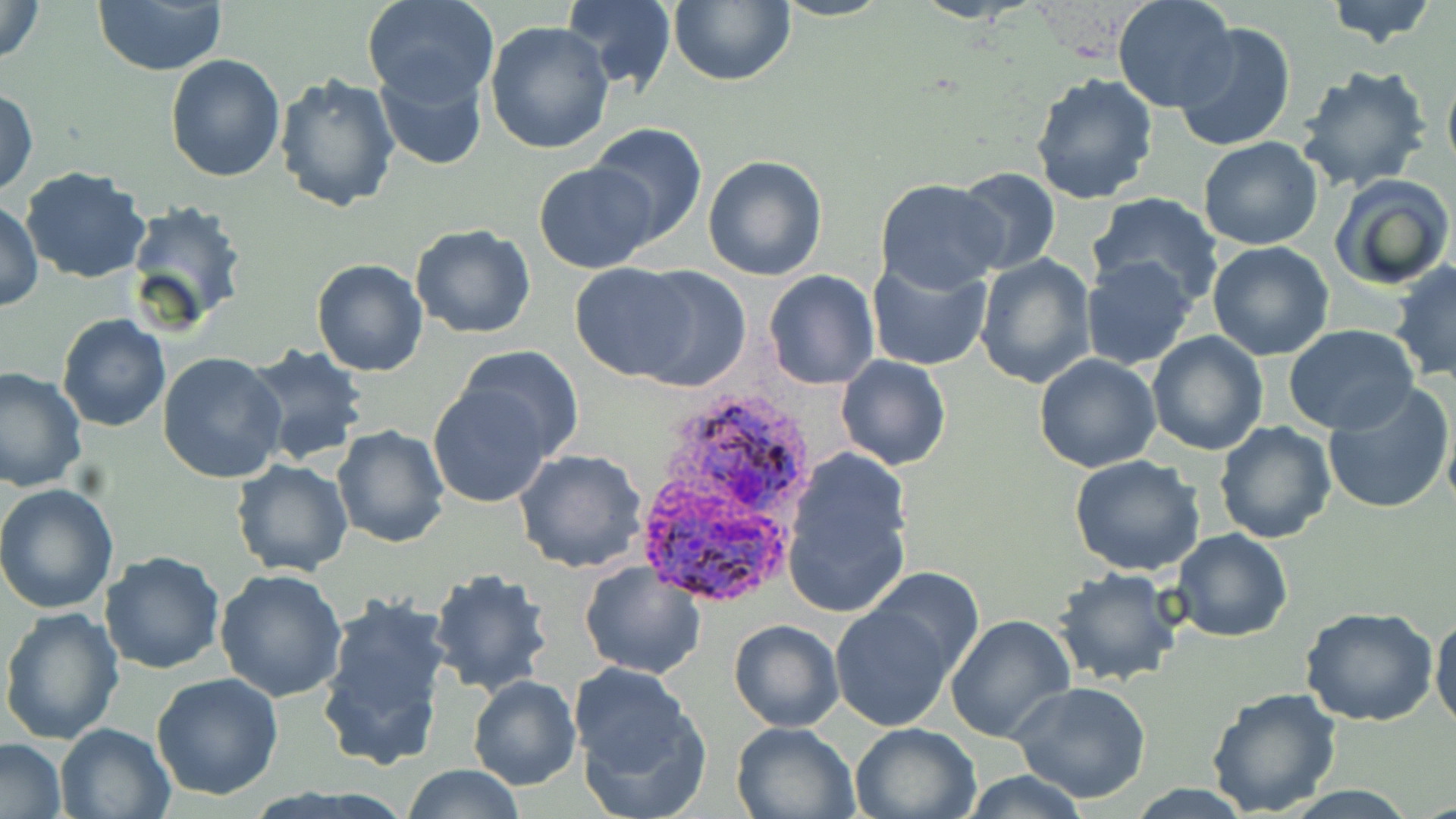
Approximate bounding boxes as (x1,y1)-(x2,y2) corner pairs in pixels. Uninfected red blood cell locations: (0,0)-(45,63), (362,0)-(499,108), (561,0)-(676,93), (669,0)-(797,88), (1323,0)-(1439,48), (1113,1)-(1238,113), (93,2)-(226,76), (484,19)-(615,155), (1172,20)-(1298,152), (164,54)-(286,182), (375,63)-(487,170), (1295,63)-(1434,192), (1442,67)-(1456,180), (1028,71)-(1160,205), (274,74)-(402,215), (0,87)-(37,198), (586,123)-(708,247), (1198,136)-(1323,250), (702,155)-(829,281), (534,162)-(658,273), (20,166)-(151,284), (953,166)-(1060,276), (1329,172)-(1455,291), (874,178)-(1007,295), (1087,192)-(1226,309), (1,199)-(45,311), (123,200)-(251,333), (409,222)-(536,340), (1206,240)-(1334,361), (975,253)-(1098,388), (866,254)-(994,371), (1079,256)-(1198,371), (311,257)-(430,377), (1389,261)-(1456,383), (570,263)-(703,381), (619,265)-(753,391), (763,269)-(881,390), (57,314)-(171,433), (1283,324)-(1423,435), (1148,332)-(1268,457), (239,341)-(370,468), (456,345)-(583,460), (158,351)-(288,484), (836,354)-(950,471), (1033,354)-(1161,474), (0,366)-(87,496), (1322,381)-(1456,515), (428,383)-(557,509), (1213,420)-(1336,544), (332,424)-(451,550), (512,449)-(649,575), (780,450)-(915,619), (1068,454)-(1207,575), (229,458)-(353,578), (0,482)-(121,614), (1172,527)-(1292,642), (99,549)-(226,675), (579,560)-(707,679), (1050,565)-(1184,688), (867,566)-(982,670), (427,567)-(554,695), (214,569)-(350,702), (316,593)-(454,770), (830,601)-(955,731), (0,606)-(124,745), (1298,607)-(1440,728), (1430,610)-(1456,732), (946,613)-(1075,742), (728,618)-(845,732), (151,672)-(284,800), (466,675)-(581,791), (1010,681)-(1153,804), (1205,686)-(1343,817), (572,696)-(711,819), (730,719)-(861,818), (55,722)-(178,818), (851,722)-(983,819), (0,738)-(67,817), (402,764)-(526,819), (954,770)-(1093,819). Plasmodium ovale-infected red blood cell locations: (670,398)-(812,509), (642,503)-(791,610). Slide-level diagnosis: Plasmodium ovale. Optical microscopy. Thin blood smear. Single field of view. May-Grünwald-Giemsa-stained preparation. Image is 1456×819 pixels. Captured at 1000x magnification.